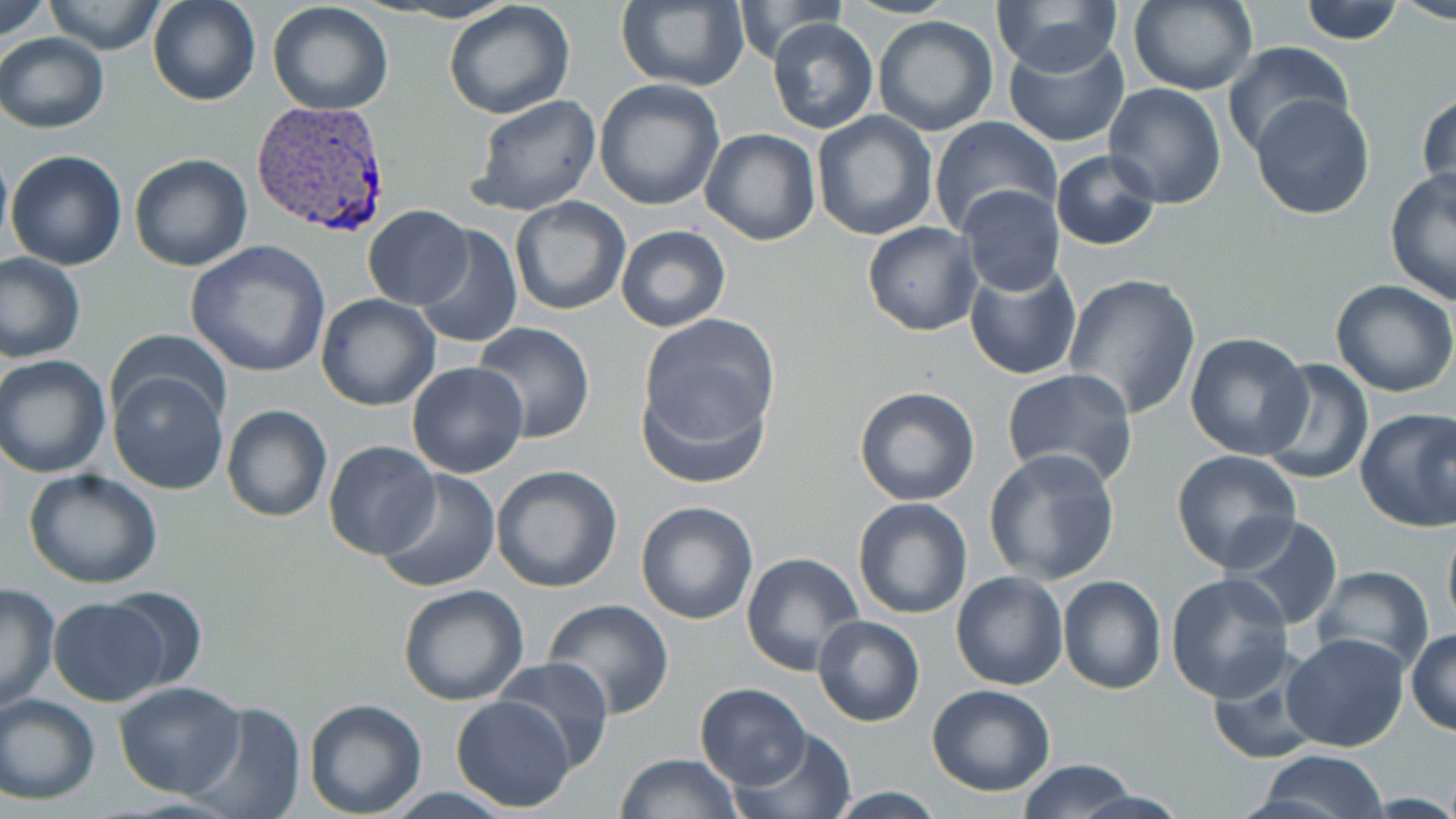

Summary:
  - Coordinate format: approximate bounding boxes as named x1/y1/x2/y2 corners in pixels
  - Plasmodium vivax-infected red blood cell locations: (x1=251, y1=99, x2=392, y2=238)
  - Uninfected red blood cell locations: (x1=1, y1=0, x2=57, y2=44), (x1=147, y1=0, x2=261, y2=106), (x1=991, y1=0, x2=1124, y2=75), (x1=1127, y1=0, x2=1257, y2=95), (x1=1388, y1=0, x2=1456, y2=24), (x1=42, y1=1, x2=166, y2=54), (x1=442, y1=1, x2=576, y2=119), (x1=616, y1=1, x2=750, y2=91), (x1=729, y1=1, x2=853, y2=65), (x1=1296, y1=1, x2=1404, y2=46), (x1=267, y1=2, x2=394, y2=116), (x1=872, y1=15, x2=1000, y2=137), (x1=767, y1=18, x2=878, y2=134), (x1=1001, y1=30, x2=1131, y2=149), (x1=0, y1=33, x2=109, y2=132), (x1=1223, y1=41, x2=1354, y2=160), (x1=593, y1=78, x2=726, y2=212), (x1=1103, y1=83, x2=1226, y2=209), (x1=1417, y1=89, x2=1455, y2=205), (x1=1249, y1=93, x2=1375, y2=220), (x1=471, y1=94, x2=602, y2=216), (x1=812, y1=111, x2=938, y2=240), (x1=930, y1=116, x2=1061, y2=237), (x1=700, y1=128, x2=819, y2=245), (x1=0, y1=142, x2=12, y2=253), (x1=6, y1=149, x2=127, y2=271), (x1=1050, y1=149, x2=1163, y2=251), (x1=129, y1=154, x2=253, y2=272), (x1=1385, y1=167, x2=1456, y2=306), (x1=957, y1=185, x2=1066, y2=298), (x1=510, y1=197, x2=630, y2=316), (x1=362, y1=205, x2=474, y2=310), (x1=861, y1=221, x2=982, y2=335), (x1=415, y1=224, x2=523, y2=350), (x1=616, y1=224, x2=730, y2=332), (x1=185, y1=241, x2=331, y2=378), (x1=0, y1=252, x2=85, y2=362), (x1=964, y1=261, x2=1082, y2=381), (x1=1062, y1=272, x2=1202, y2=420), (x1=1330, y1=280, x2=1456, y2=398), (x1=315, y1=294, x2=439, y2=410), (x1=636, y1=316, x2=780, y2=477), (x1=473, y1=322, x2=594, y2=442), (x1=109, y1=330, x2=232, y2=430), (x1=1185, y1=333, x2=1313, y2=459), (x1=1, y1=355, x2=113, y2=476), (x1=1258, y1=358, x2=1375, y2=485), (x1=406, y1=362, x2=529, y2=479), (x1=108, y1=367, x2=230, y2=496), (x1=1002, y1=369, x2=1138, y2=489), (x1=853, y1=386, x2=981, y2=507), (x1=221, y1=404, x2=332, y2=523), (x1=1353, y1=408, x2=1456, y2=533), (x1=323, y1=440, x2=442, y2=560), (x1=983, y1=448, x2=1121, y2=585), (x1=1170, y1=449, x2=1302, y2=573), (x1=490, y1=465, x2=622, y2=593), (x1=25, y1=470, x2=164, y2=588), (x1=376, y1=470, x2=501, y2=593), (x1=853, y1=496, x2=973, y2=619), (x1=635, y1=500, x2=759, y2=625), (x1=1226, y1=513, x2=1344, y2=632), (x1=1442, y1=519, x2=1456, y2=636), (x1=741, y1=552, x2=863, y2=675), (x1=1312, y1=565, x2=1434, y2=675), (x1=951, y1=571, x2=1069, y2=692), (x1=1165, y1=573, x2=1294, y2=702), (x1=1057, y1=574, x2=1167, y2=694), (x1=0, y1=581, x2=59, y2=712), (x1=397, y1=583, x2=529, y2=704), (x1=98, y1=587, x2=211, y2=690), (x1=48, y1=598, x2=169, y2=707), (x1=543, y1=598, x2=676, y2=719), (x1=813, y1=613, x2=925, y2=727), (x1=1407, y1=630, x2=1456, y2=736), (x1=1280, y1=632, x2=1409, y2=753), (x1=1207, y1=654, x2=1325, y2=767), (x1=494, y1=656, x2=615, y2=772), (x1=114, y1=681, x2=247, y2=798), (x1=694, y1=682, x2=811, y2=790), (x1=928, y1=684, x2=1057, y2=797), (x1=0, y1=693, x2=101, y2=804), (x1=450, y1=695, x2=576, y2=813), (x1=303, y1=698, x2=427, y2=818), (x1=183, y1=699, x2=308, y2=819), (x1=729, y1=729, x2=858, y2=819), (x1=1255, y1=749, x2=1389, y2=819), (x1=615, y1=753, x2=743, y2=818), (x1=1014, y1=759, x2=1138, y2=819), (x1=822, y1=787, x2=950, y2=818), (x1=1068, y1=787, x2=1192, y2=819)
  - Slide-level diagnosis: Plasmodium vivax
  - Magnification: 1000x
  - Modality: optical microscopy
  - Field of view: one of a larger specimen
  - Image size: 1456×819 pixels
  - Stain: May-Grünwald-Giemsa
  - Preparation: thin blood film